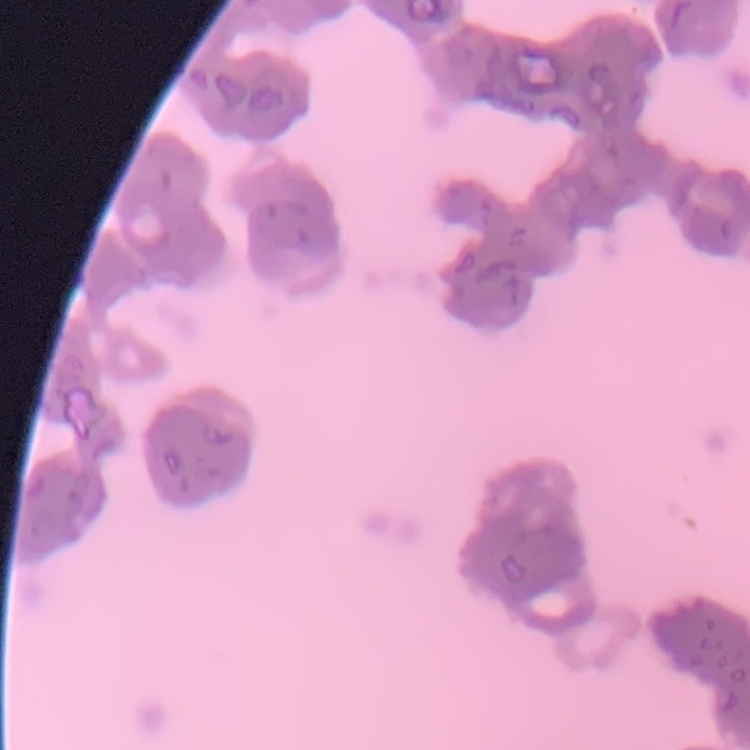
The red blood cells show rouleaux formation. Square crop of a larger photomicrograph. Stained with either Field's or Giemsa. Thin peripheral smear.